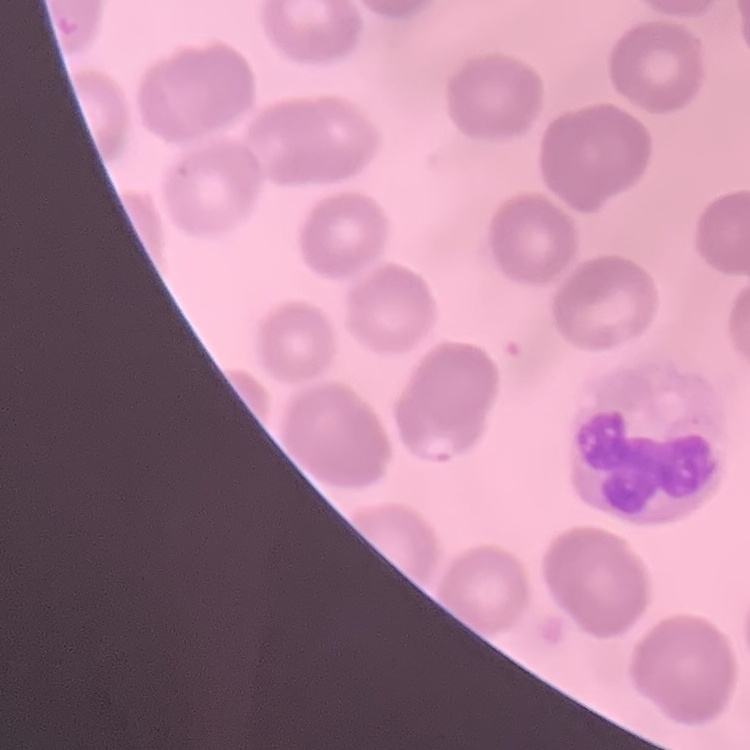

red blood cell morphology = no rouleaux formation
preparation = thin blood film
stain = Field's or Giemsa
image type = square crop of a larger photomicrograph